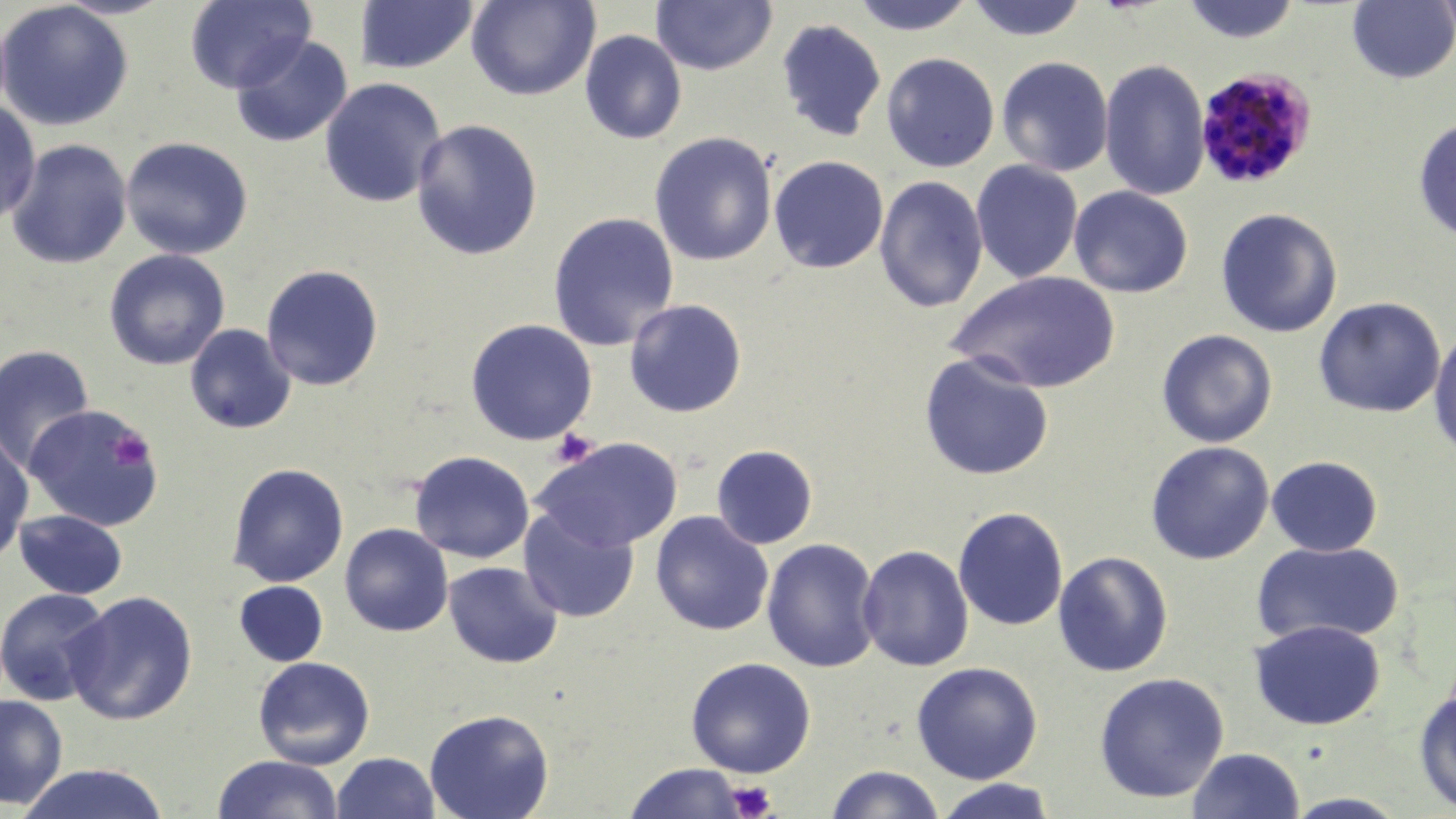
slide-level diagnosis = Plasmodium malariae
image size = 1456×819 pixels
stain = May-Grünwald-Giemsa
preparation = thin blood film
field of view = one of a larger specimen
modality = light microscopy
uninfected red blood cell locations = approximate bounding boxes as [x1, y1, x2, y2] in pixels: [184, 0, 315, 93], [467, 0, 600, 102], [651, 0, 777, 76], [850, 0, 977, 36], [965, 0, 1088, 41], [1179, 0, 1302, 44], [1431, 0, 1456, 45], [0, 1, 135, 131], [354, 1, 478, 74], [1347, 1, 1455, 84], [777, 18, 885, 142], [580, 30, 687, 144], [230, 34, 353, 147], [881, 52, 1000, 172], [996, 56, 1114, 177], [1098, 58, 1211, 201], [319, 77, 447, 208], [0, 99, 41, 225], [1413, 118, 1456, 241], [411, 119, 543, 260], [648, 131, 777, 266], [121, 136, 254, 260], [7, 139, 132, 269], [768, 155, 889, 274], [971, 160, 1083, 284], [874, 175, 988, 313], [1069, 185, 1193, 297], [1215, 207, 1343, 338], [547, 211, 680, 351], [103, 249, 230, 370], [261, 264, 384, 391], [946, 270, 1121, 394], [1312, 296, 1446, 418], [624, 298, 748, 417], [464, 318, 598, 446], [185, 323, 296, 434], [1428, 325, 1456, 462], [1156, 329, 1278, 448], [0, 344, 96, 475], [918, 352, 1055, 481], [23, 404, 165, 531], [0, 434, 34, 565], [534, 437, 684, 552], [1145, 441, 1274, 565], [711, 444, 818, 549], [409, 450, 535, 563], [1266, 455, 1383, 557], [227, 462, 349, 587], [518, 505, 639, 623], [952, 507, 1069, 631], [14, 509, 127, 600], [650, 511, 774, 635], [339, 523, 454, 636], [761, 538, 881, 673], [1250, 540, 1405, 647], [857, 544, 974, 672], [1053, 551, 1174, 677], [443, 560, 563, 668], [234, 581, 328, 666], [0, 588, 114, 706], [63, 591, 198, 725], [1249, 619, 1386, 730], [253, 656, 375, 769], [685, 657, 816, 778], [911, 661, 1044, 784], [1093, 672, 1230, 802], [1413, 687, 1456, 816], [0, 694, 68, 809], [424, 708, 554, 819], [1187, 747, 1305, 819], [331, 752, 440, 819], [214, 754, 343, 819], [17, 763, 170, 819], [623, 763, 746, 819], [825, 764, 945, 819], [931, 778, 1059, 819], [1279, 792, 1412, 818]
Plasmodium malariae-infected red blood cell locations = approximate bounding boxes as [x1, y1, x2, y2] in pixels: [1194, 67, 1317, 190]
magnification = 1000x
platelet locations = approximate bounding boxes as [x1, y1, x2, y2] in pixels: [550, 428, 598, 469], [109, 429, 154, 471], [727, 780, 778, 819]